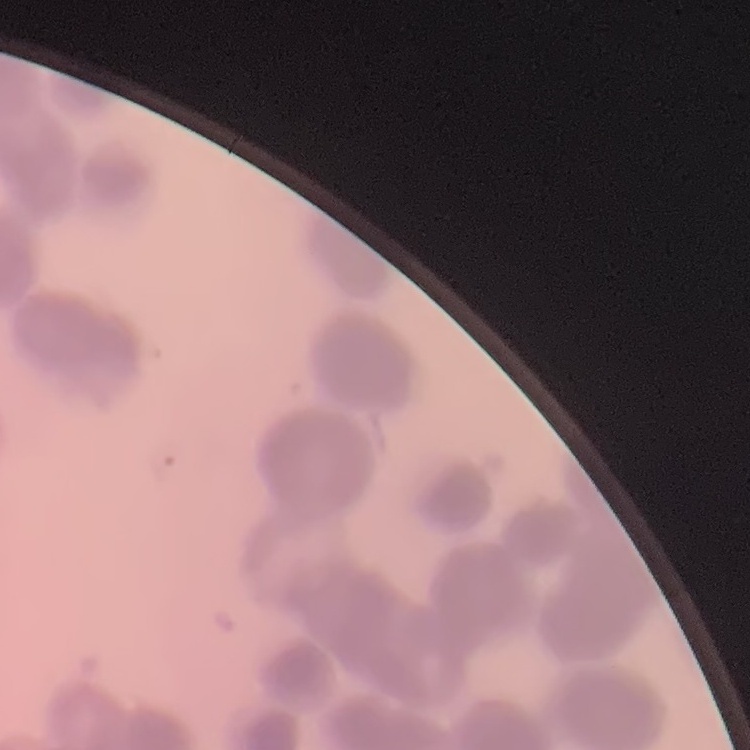
Summary:
  - Red blood cell morphology: rouleaux formation
  - Stain: Field's or Giemsa
  - Image type: one tile cut from a larger photomicrograph
  - Preparation: thin blood film